Locate every malaria parasite and identify its life-cycle stage.
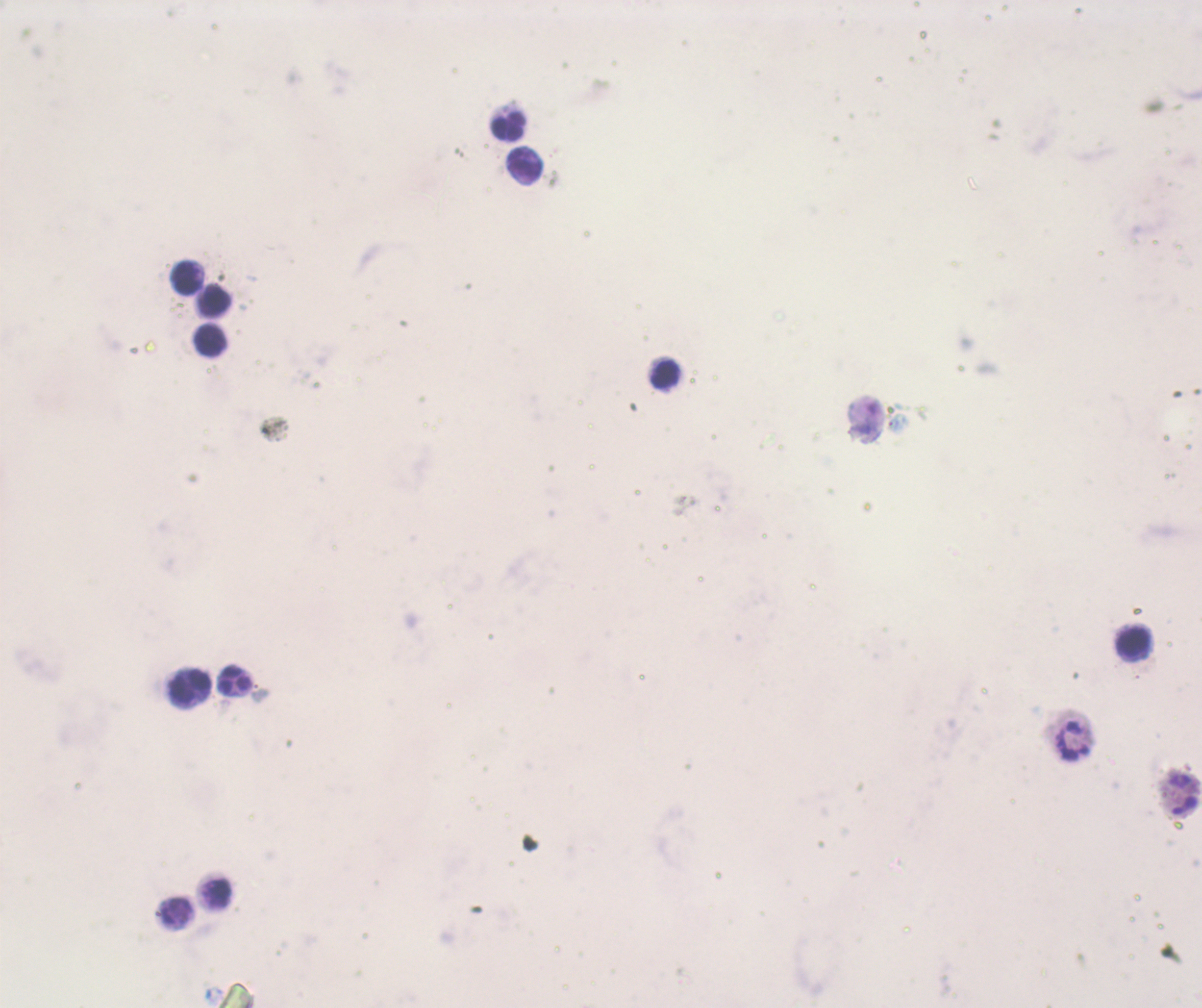
Approximate centers as [x, y] in pixels.
Trophozoites: [898, 423].
No schizont or gametocyte forms observed.

Approximate centers as [x, y] in pixels. Leukocyte locations: [508, 125], [525, 165], [187, 277], [214, 302], [211, 340], [665, 375], [1134, 643], [234, 681], [191, 687], [1071, 741], [1181, 796], [215, 894]. Image is 1202×1008 pixels. One field from this slide. Thick blood smear. Coloration quality: bad. Romanowsky stain. Captured at 100x magnification. Previously used in a real diagnosis. Background quality: unsatisfactory.